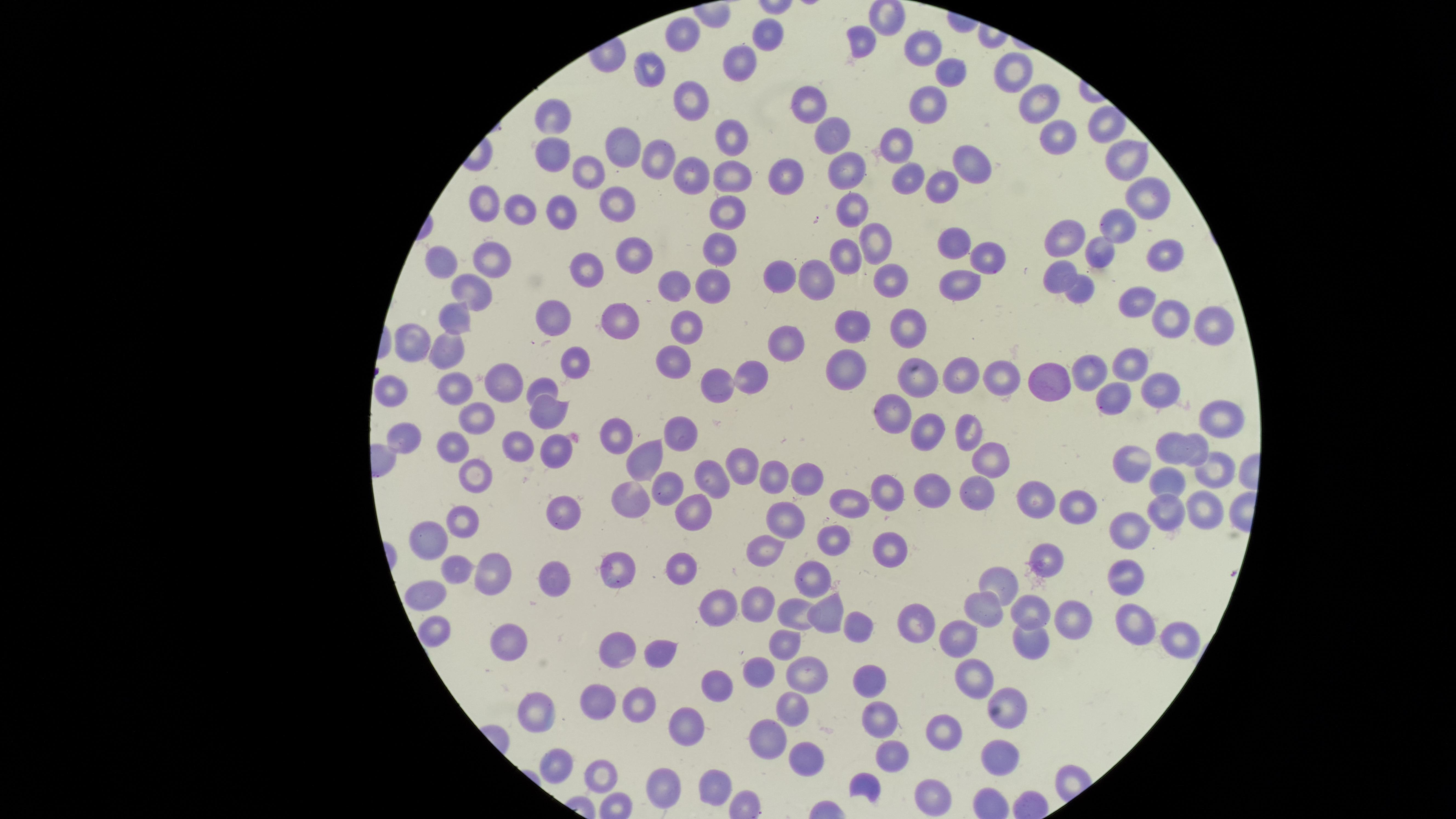

Approximate marker points as [x, y] in pixels. Uninfected red blood cells: [769, 27], [684, 37], [863, 41], [924, 48], [740, 58], [1008, 66], [653, 68], [948, 73], [689, 100], [1038, 100], [931, 106], [811, 107], [552, 116], [1107, 124], [829, 130], [1056, 134], [734, 138], [626, 144], [899, 145], [556, 146], [664, 155], [1122, 157], [847, 166], [963, 166], [790, 172], [590, 173], [693, 174], [910, 175], [734, 176], [941, 183], [1156, 190], [488, 197], [616, 200], [523, 202], [851, 207], [565, 209], [728, 209], [1122, 229], [1065, 238], [870, 241], [954, 242], [721, 248], [845, 252], [1098, 252], [1165, 252], [634, 255], [988, 255], [498, 257], [450, 258], [593, 264], [783, 272], [1052, 275], [819, 277], [960, 279], [891, 280], [674, 283], [715, 286], [1079, 291], [474, 292], [1132, 301], [560, 313], [460, 316], [1170, 318], [1205, 321], [618, 323], [852, 325], [909, 326], [681, 329], [791, 337], [414, 344], [448, 347], [573, 360], [675, 360], [845, 366], [1125, 366], [1012, 369], [1081, 372], [958, 373], [918, 374], [746, 375], [1057, 379], [453, 382], [545, 384], [718, 385], [1151, 386], [388, 388], [499, 395], [1105, 399], [478, 409], [891, 410], [1220, 413], [550, 415], [967, 424], [678, 430], [929, 431], [613, 432], [458, 440], [406, 441], [1196, 444], [518, 446], [1172, 448], [555, 450], [993, 459], [748, 462], [1136, 462], [645, 464], [1209, 465], [475, 473], [806, 475], [708, 480], [776, 480], [1165, 481], [890, 482], [934, 486], [671, 488], [974, 491], [628, 492], [851, 502], [1042, 502], [1210, 504], [1078, 509], [693, 510], [566, 511], [1169, 512], [464, 514], [778, 520], [1137, 527], [435, 534], [835, 539], [762, 550], [889, 554], [1042, 561], [683, 565], [493, 566], [457, 569], [619, 571], [818, 571], [1131, 575], [551, 576], [1002, 583], [424, 592], [714, 599], [756, 599], [1032, 607], [985, 608], [796, 611], [825, 617], [919, 620], [1066, 621], [1135, 622], [443, 626], [855, 627], [960, 634], [1031, 639], [1178, 639], [512, 642], [783, 643], [620, 648], [657, 656], [760, 667], [810, 667], [970, 676], [876, 682], [716, 687], [1011, 701], [599, 703], [791, 708], [640, 711], [537, 713], [883, 724], [940, 727], [690, 734], [772, 738], [894, 756], [1006, 759], [809, 760], [560, 764], [602, 774], [721, 784], [658, 785], [861, 785], [936, 794]. Circular visible region. Image is 1456×819 pixels. Thin smear of blood. Presence: no malaria parasites detected. Photographed with a smartphone camera through the microscope eyepiece. Giemsa stain. Single field of view.